Assess the morphology of the red blood cells.
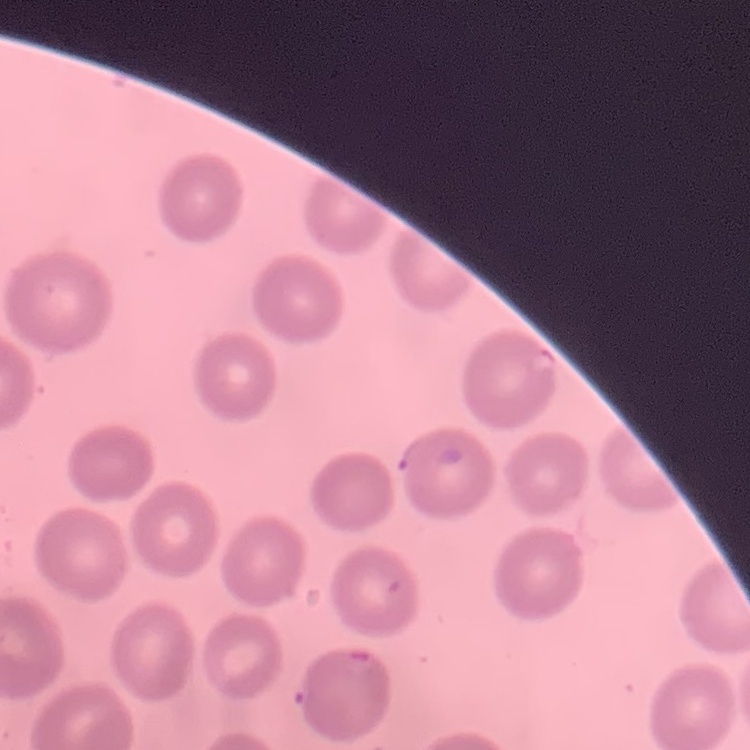

They show no rouleaux formation.

Square crop of a larger photomicrograph. Thin blood film. Field's or Giemsa stain.